Classify this cell by malaria status.
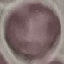
Uninfected.

stain = Giemsa
image type = cell patch, automatically extracted from a larger field of view and resized to 64 × 64 pixels
preparation = thin blood film
capture = smartphone camera at the microscope eyepiece